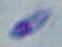
Toxoplasma gondii is seen. Photomicrograph. Captured at 1000x magnification.